Classify this cell by malaria status.
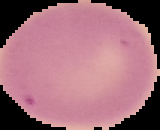
Uninfected.

Summary:
  - Preparation: thin blood film
  - Image size: 160×130 pixels
  - Image type: segmented cell region with the area outside set to black